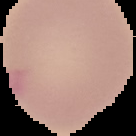

Summary:
  - Image size: 136×136 pixels
  - Preparation: thin blood film
  - Image type: segmented cell region on a black background
  - Malaria status: uninfected